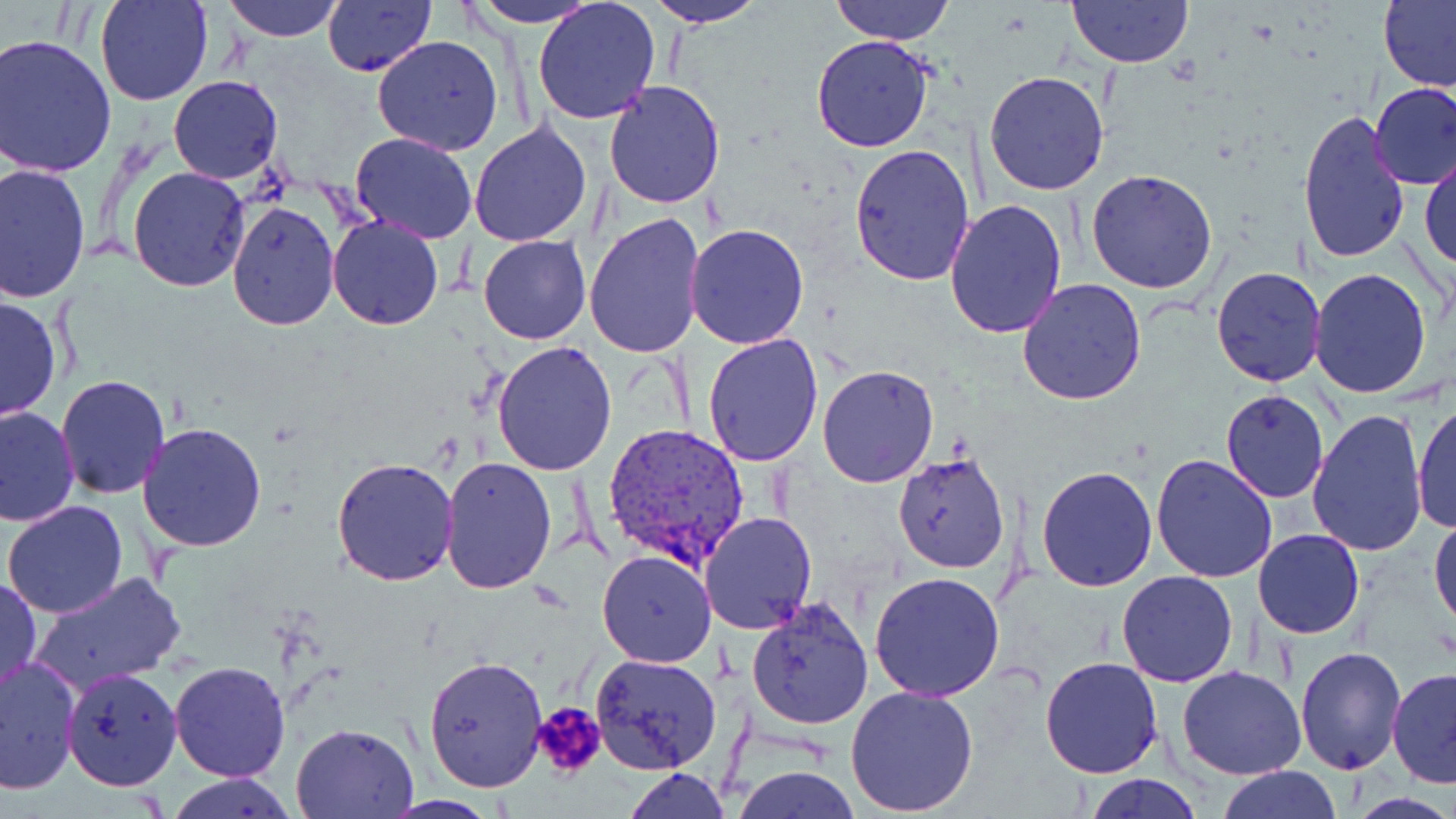

Approximate bounding boxes as named x1/y1/x2/y2 corners in pixels. Uninfected red blood cell locations: (x1=95, y1=0, x2=213, y2=106), (x1=321, y1=0, x2=434, y2=76), (x1=465, y1=0, x2=604, y2=27), (x1=643, y1=0, x2=767, y2=29), (x1=832, y1=0, x2=955, y2=45), (x1=1067, y1=0, x2=1192, y2=68), (x1=220, y1=1, x2=347, y2=41), (x1=1379, y1=1, x2=1456, y2=93), (x1=532, y1=2, x2=660, y2=125), (x1=1, y1=34, x2=120, y2=178), (x1=372, y1=35, x2=504, y2=157), (x1=810, y1=36, x2=934, y2=153), (x1=984, y1=70, x2=1110, y2=195), (x1=168, y1=75, x2=283, y2=185), (x1=603, y1=81, x2=726, y2=209), (x1=1369, y1=81, x2=1456, y2=189), (x1=1297, y1=108, x2=1411, y2=266), (x1=469, y1=121, x2=594, y2=245), (x1=350, y1=132, x2=478, y2=242), (x1=849, y1=144, x2=977, y2=288), (x1=1420, y1=151, x2=1455, y2=274), (x1=0, y1=160, x2=93, y2=304), (x1=127, y1=167, x2=251, y2=291), (x1=1085, y1=169, x2=1217, y2=294), (x1=226, y1=199, x2=340, y2=331), (x1=945, y1=199, x2=1068, y2=340), (x1=584, y1=213, x2=710, y2=361), (x1=327, y1=216, x2=445, y2=329), (x1=686, y1=223, x2=812, y2=350), (x1=478, y1=235, x2=590, y2=345), (x1=1211, y1=266, x2=1325, y2=388), (x1=1310, y1=268, x2=1432, y2=397), (x1=1018, y1=279, x2=1147, y2=405), (x1=1, y1=294, x2=62, y2=423), (x1=701, y1=333, x2=824, y2=468), (x1=491, y1=340, x2=619, y2=475), (x1=817, y1=364, x2=940, y2=487), (x1=57, y1=373, x2=170, y2=499), (x1=1218, y1=387, x2=1330, y2=503), (x1=1411, y1=400, x2=1455, y2=536), (x1=0, y1=406, x2=80, y2=530), (x1=1308, y1=407, x2=1429, y2=558), (x1=138, y1=421, x2=269, y2=552), (x1=892, y1=450, x2=1011, y2=573), (x1=1150, y1=454, x2=1278, y2=582), (x1=439, y1=457, x2=557, y2=594), (x1=331, y1=458, x2=459, y2=586), (x1=1036, y1=464, x2=1159, y2=591), (x1=4, y1=501, x2=129, y2=620), (x1=701, y1=511, x2=817, y2=633), (x1=1429, y1=512, x2=1456, y2=635), (x1=1253, y1=529, x2=1363, y2=639), (x1=597, y1=550, x2=716, y2=668), (x1=25, y1=569, x2=189, y2=698), (x1=869, y1=571, x2=1007, y2=701), (x1=1115, y1=571, x2=1238, y2=688), (x1=0, y1=576, x2=41, y2=698), (x1=745, y1=598, x2=874, y2=730), (x1=1295, y1=644, x2=1408, y2=775), (x1=590, y1=651, x2=723, y2=774), (x1=0, y1=654, x2=80, y2=794), (x1=424, y1=656, x2=548, y2=792), (x1=1040, y1=656, x2=1164, y2=777), (x1=169, y1=661, x2=291, y2=781), (x1=1177, y1=665, x2=1306, y2=780), (x1=62, y1=668, x2=181, y2=790), (x1=1387, y1=668, x2=1456, y2=789), (x1=845, y1=683, x2=980, y2=816), (x1=291, y1=721, x2=419, y2=817), (x1=731, y1=764, x2=862, y2=819), (x1=1216, y1=765, x2=1341, y2=819), (x1=620, y1=768, x2=730, y2=819), (x1=1086, y1=772, x2=1202, y2=818), (x1=166, y1=774, x2=299, y2=818). Platelet locations: (x1=532, y1=699, x2=608, y2=781). Plasmodium vivax-infected red blood cell locations: (x1=604, y1=422, x2=750, y2=574). Slide-level diagnosis: Plasmodium vivax. One field of a larger specimen. 1000x magnification. Light microscopy. May-Grünwald-Giemsa-stained preparation. Thin blood film. Image is 1456×819 pixels.